Assess the morphology of the red blood cells.
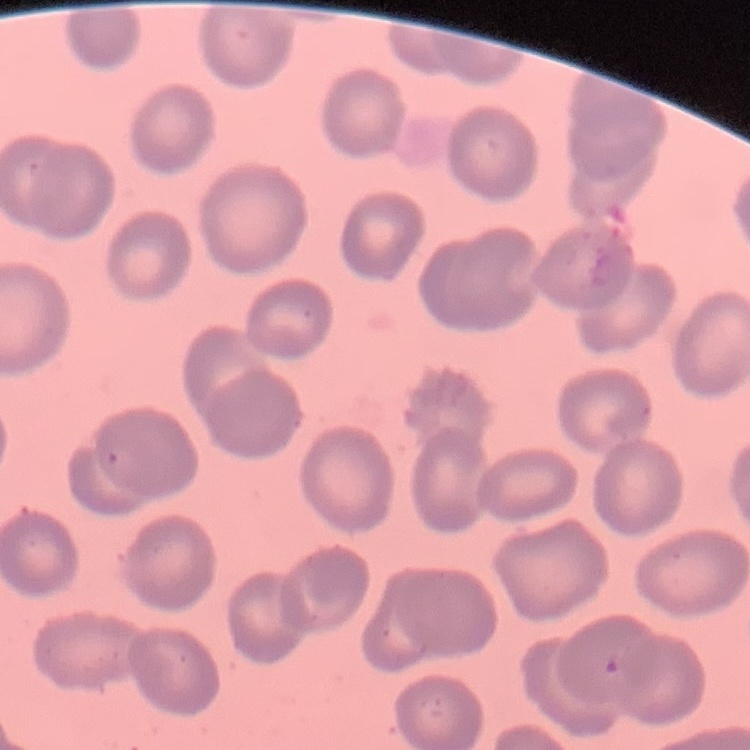

No rouleaux formation.

stain = Field's or Giemsa
preparation = thin blood film
image type = square crop of a larger photomicrograph